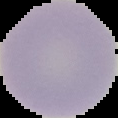
Summary:
  - Image type: segmented cell region on a black background
  - Malaria status: uninfected
  - Image size: 118×118 pixels
  - Preparation: thin blood film